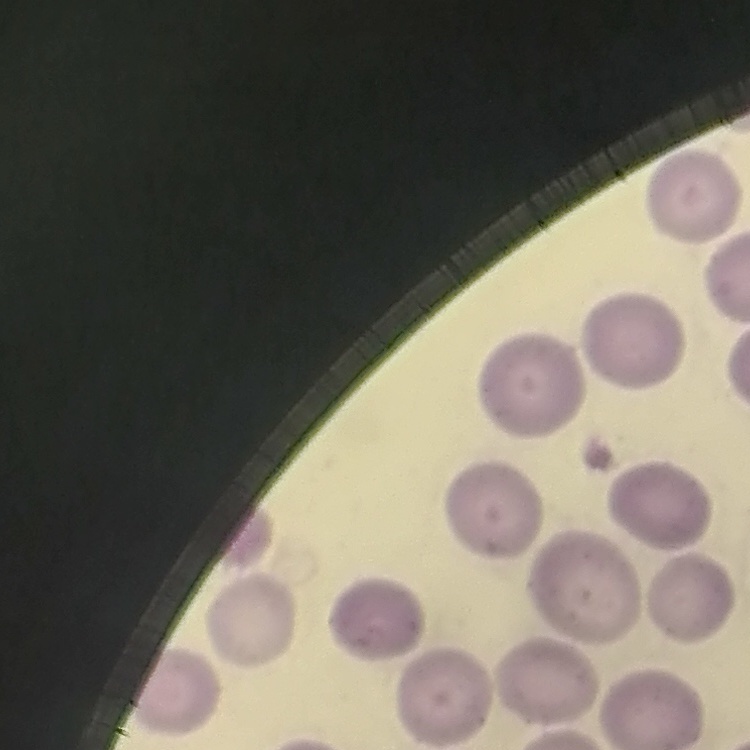

The red blood cells show no rouleaux formation. Stained with either Field's or Giemsa. Thin peripheral smear. Square crop of a larger photomicrograph.